Name the parasite shown.
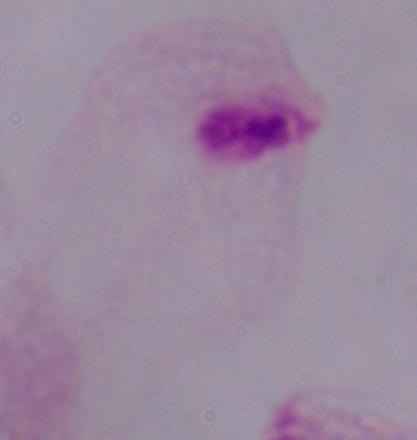

A trichomonad.

1000x magnification. Micrograph.